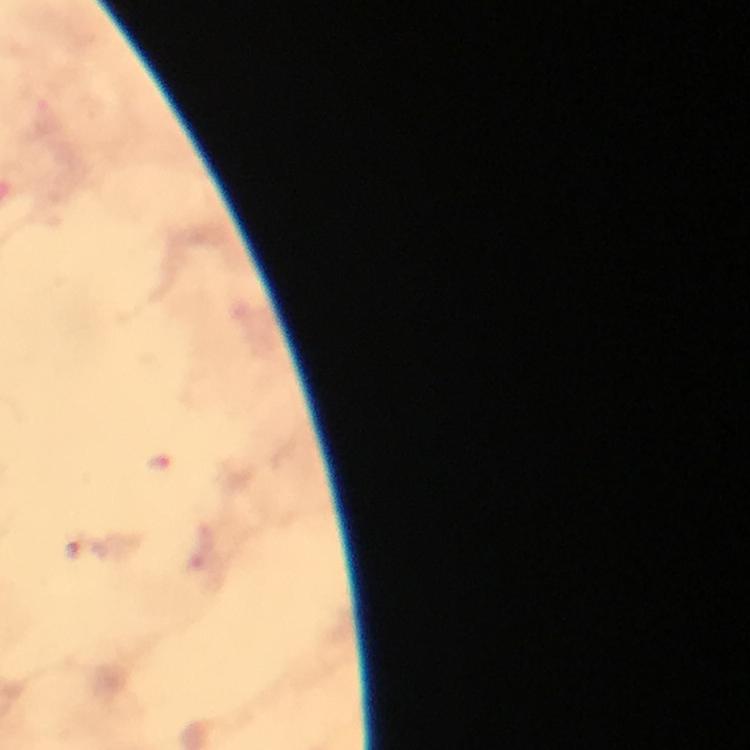 Approximate centers as (x, y) in pixels. Malaria parasite locations: (159, 464), (73, 549). Photographed with a smartphone mounted on the microscope. Thick blood smear. Image is 750×750 pixels. Giemsa stain. Immersion oil was used. From a diagnostic examination for malaria. Cropped region of a single field of view. At 100x magnification.